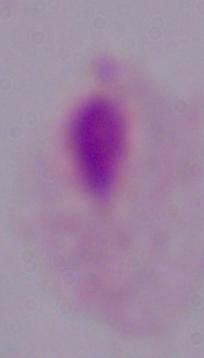
{
  "magnification": "1000x",
  "identification": "trichomonad",
  "modality": "photomicrograph"
}